Give the extent of all Plasmodium parasites.
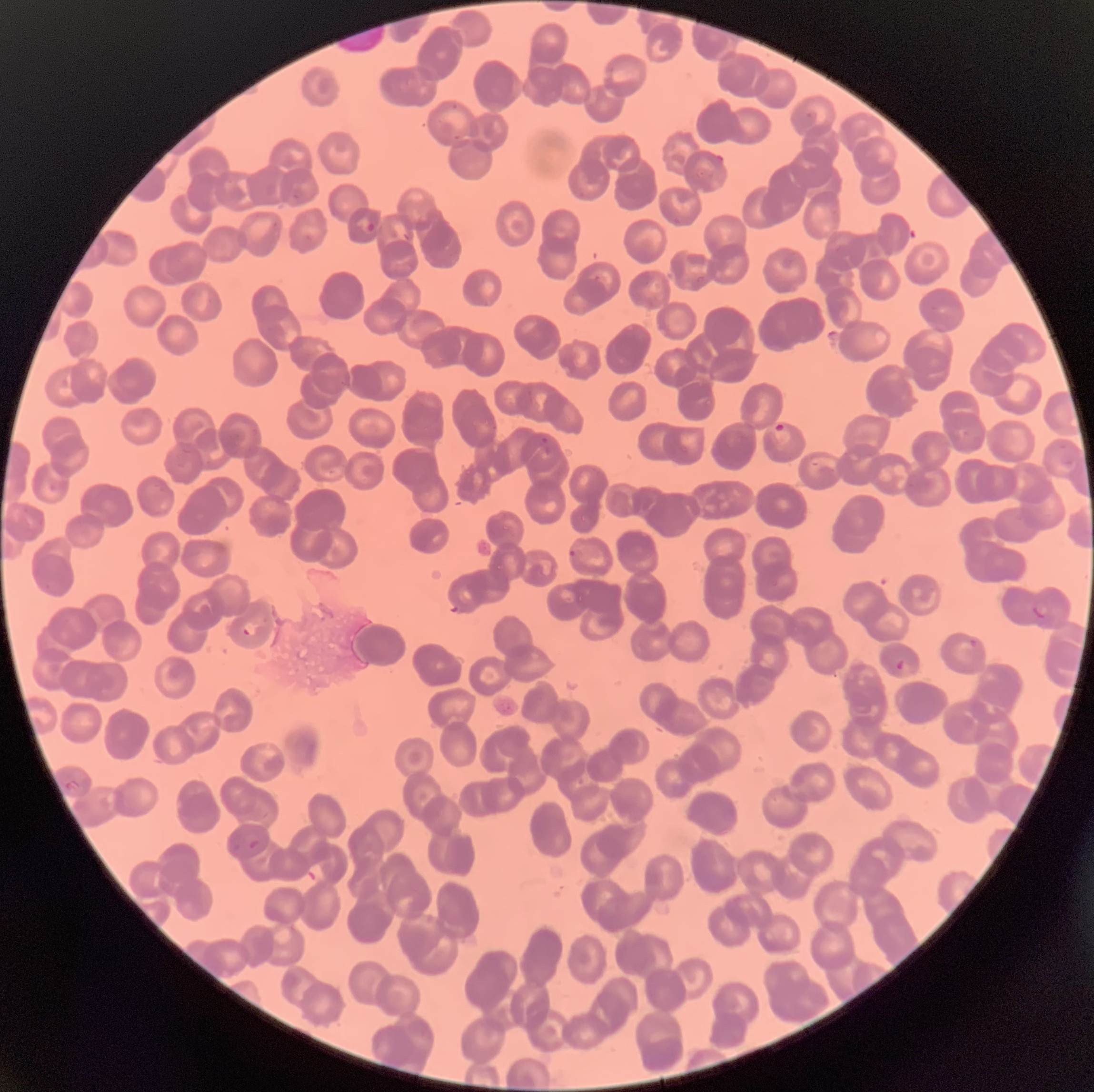
Approximate bounding boxes as named x1/y1/x2/y2 corners in pixels.
Plasmodium parasites: (x1=356, y1=216, x2=377, y2=234), (x1=773, y1=423, x2=791, y2=447), (x1=541, y1=436, x2=556, y2=456), (x1=566, y1=548, x2=583, y2=561), (x1=1032, y1=603, x2=1051, y2=619), (x1=242, y1=621, x2=260, y2=637), (x1=968, y1=638, x2=979, y2=650), (x1=895, y1=658, x2=912, y2=673), (x1=63, y1=780, x2=82, y2=794).

{
  "modality": "light microscopy",
  "preparation": "thin blood smear",
  "image_size": "1094×1092 pixels",
  "red_blood_cell_morphology": "rouleaux formation"
}